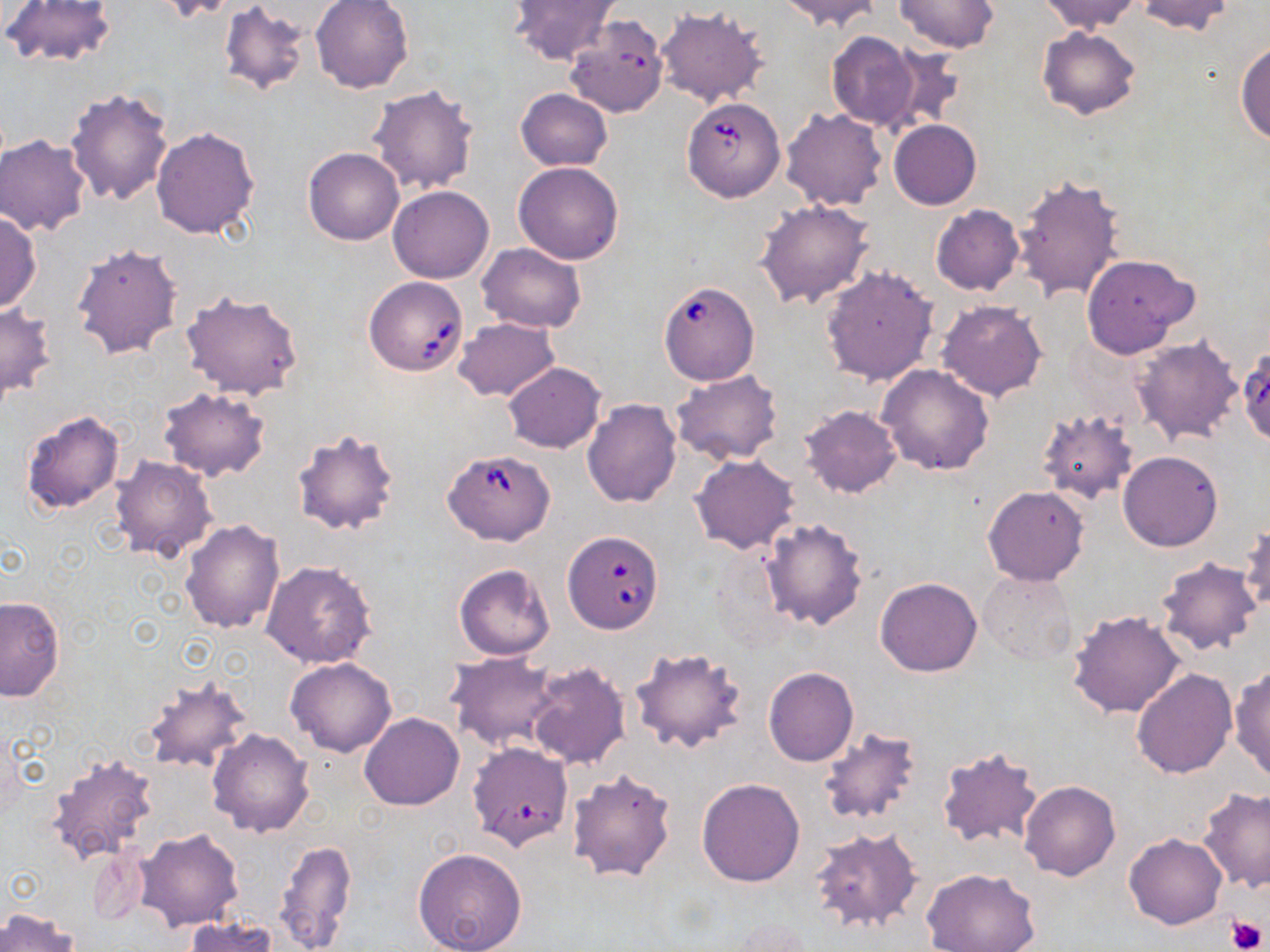
slide-level diagnosis = Babesia divergens
uninfected red blood cell locations = approximate bounding boxes as [x1, y1, x2, y2] in pixels: [1, 0, 118, 69], [157, 0, 240, 22], [310, 0, 413, 94], [507, 0, 620, 67], [777, 0, 883, 32], [896, 0, 999, 52], [1038, 0, 1141, 34], [1136, 0, 1236, 37], [217, 4, 311, 98], [655, 6, 769, 108], [1036, 26, 1141, 120], [826, 31, 921, 132], [1236, 40, 1270, 144], [882, 48, 966, 134], [367, 84, 478, 194], [65, 87, 176, 208], [515, 88, 612, 171], [781, 108, 888, 212], [0, 113, 165, 228], [889, 119, 981, 209], [151, 126, 260, 240], [0, 136, 90, 236], [303, 147, 404, 246], [513, 161, 625, 264], [1011, 174, 1125, 304], [387, 186, 494, 283], [755, 198, 876, 309], [930, 204, 1024, 296], [0, 212, 41, 312], [71, 242, 184, 361], [476, 243, 586, 332], [1081, 254, 1198, 358], [821, 266, 938, 386], [179, 290, 306, 398], [937, 300, 1047, 402], [0, 304, 58, 405], [452, 317, 559, 402], [1131, 335, 1243, 446], [502, 362, 605, 453], [877, 363, 993, 475], [671, 370, 785, 466], [157, 386, 271, 481], [581, 398, 681, 508], [800, 405, 902, 497], [20, 409, 126, 516], [1036, 410, 1139, 507], [290, 427, 401, 537], [1118, 451, 1222, 552], [111, 455, 219, 562], [691, 455, 800, 554], [982, 486, 1089, 586], [760, 517, 868, 630], [179, 519, 284, 634], [1239, 521, 1270, 617], [1155, 558, 1262, 656], [261, 560, 377, 669], [453, 564, 556, 661], [978, 571, 1077, 665], [875, 577, 983, 677], [0, 596, 65, 701], [1067, 610, 1186, 718], [630, 646, 748, 755], [447, 652, 561, 751], [285, 657, 397, 758], [526, 661, 630, 770], [1229, 664, 1270, 783], [763, 667, 858, 766], [1131, 670, 1236, 778], [139, 675, 253, 774], [360, 713, 463, 809], [818, 725, 927, 828], [207, 728, 315, 838], [936, 746, 1045, 852], [46, 751, 158, 867], [566, 767, 678, 883], [696, 777, 806, 886], [1021, 781, 1120, 880], [1197, 785, 1270, 892], [133, 827, 245, 933], [809, 827, 924, 935], [1124, 834, 1226, 930], [275, 838, 357, 952], [411, 847, 528, 952], [921, 868, 1041, 952], [0, 906, 78, 952], [183, 916, 276, 952], [722, 919, 817, 951]
magnification = 1000x
modality = optical microscopy
preparation = thin blood smear
Babesia divergens-infected red blood cell locations = approximate bounding boxes as [x1, y1, x2, y2] in pixels: [566, 16, 668, 116], [681, 95, 785, 202], [364, 275, 469, 377], [657, 281, 760, 385], [1237, 349, 1270, 446], [444, 449, 555, 544], [563, 530, 663, 632], [467, 741, 574, 849]
platelet locations = approximate bounding boxes as [x1, y1, x2, y2] in pixels: [1229, 917, 1266, 950]
image size = 1270×952 pixels
field of view = one of a larger specimen
stain = May-Grünwald-Giemsa